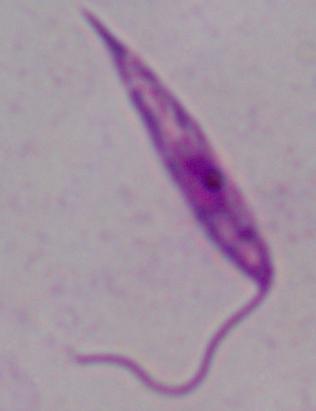

A Leishmania parasite is shown. Photomicrograph. 1000x magnification.